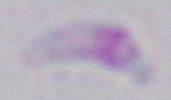
Summary:
  - Identification: Toxoplasma gondii
  - Magnification: 1000x
  - Modality: micrograph